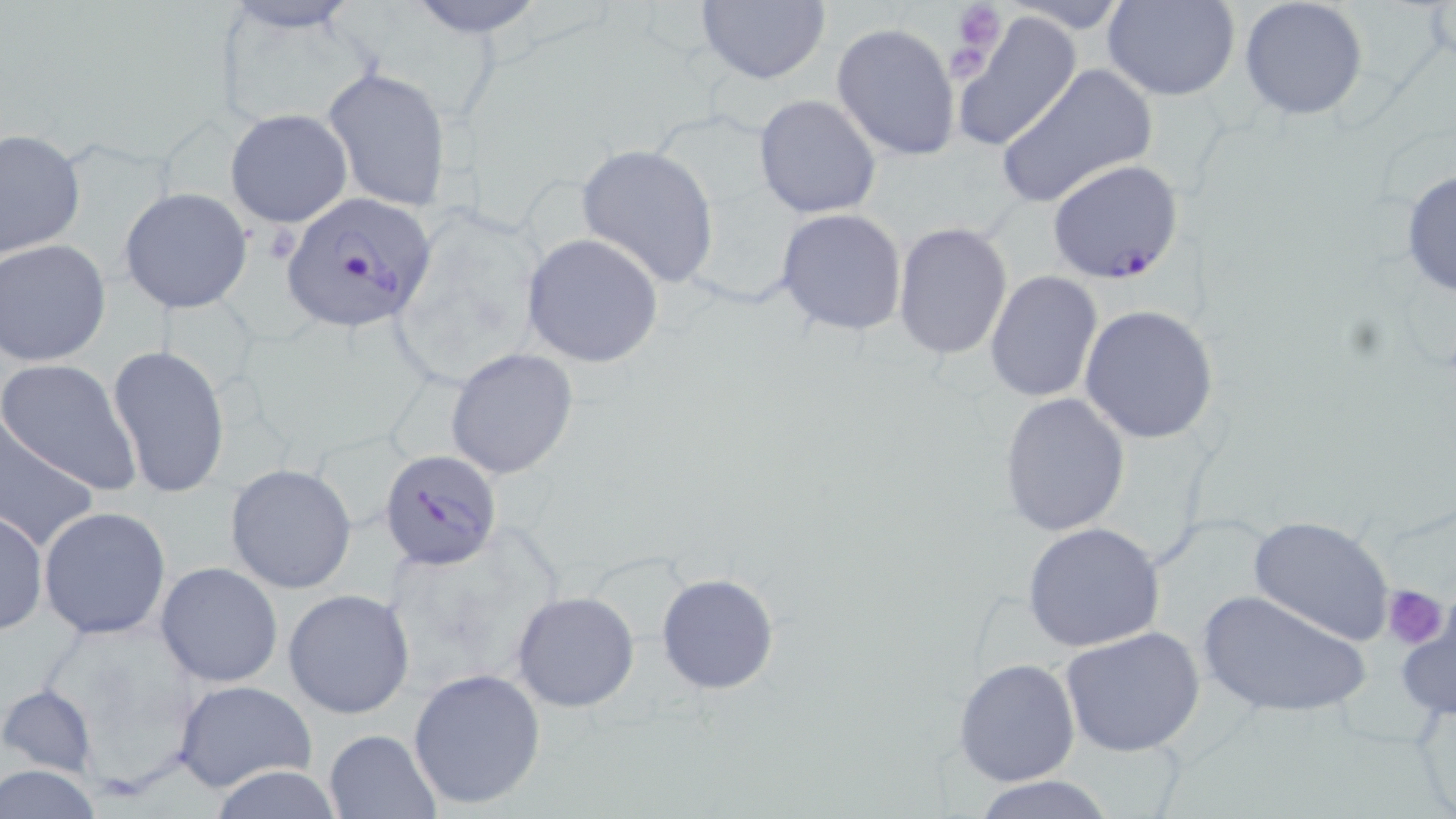
Approximate bounding boxes as (x1, y1, x2, y2) in pixels. Uninfected red blood cell locations: (404, 0, 549, 38), (692, 0, 833, 89), (1004, 0, 1133, 34), (1103, 0, 1242, 101), (1238, 0, 1369, 120), (951, 10, 1083, 150), (831, 23, 962, 162), (995, 64, 1158, 208), (323, 66, 453, 212), (754, 94, 881, 218), (225, 108, 352, 227), (1, 128, 86, 258), (576, 143, 719, 289), (1401, 169, 1456, 301), (119, 187, 252, 314), (776, 209, 908, 337), (892, 221, 1014, 360), (520, 232, 665, 369), (2, 239, 110, 365), (985, 270, 1104, 404), (1079, 304, 1219, 444), (108, 345, 231, 499), (446, 348, 578, 479), (1, 358, 142, 494), (999, 392, 1130, 536), (0, 418, 101, 552), (226, 464, 358, 595), (38, 506, 172, 640), (0, 510, 47, 634), (1248, 515, 1396, 646), (1021, 522, 1166, 652), (155, 561, 283, 687), (656, 572, 778, 695), (284, 589, 417, 719), (511, 590, 640, 712), (1198, 590, 1370, 719), (1393, 594, 1456, 728), (1060, 626, 1207, 759), (953, 657, 1081, 787), (407, 669, 546, 810), (171, 679, 319, 794), (1, 683, 100, 782), (324, 728, 441, 818), (1, 765, 107, 817), (202, 765, 352, 819), (972, 775, 1115, 819). Platelet locations: (951, 1, 1007, 62), (1383, 582, 1448, 649). Plasmodium falciparum-infected red blood cell locations: (1047, 159, 1184, 284), (279, 189, 440, 333), (379, 449, 503, 572). Slide-level diagnosis: Plasmodium falciparum. Image is 1456×819 pixels. 1000x magnification. Single field of view. Thin blood smear. May-Grünwald-Giemsa stain. Optical microscopy.